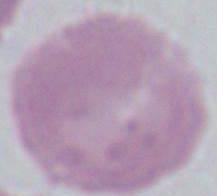
Summary:
  - Magnification: 1000x
  - Modality: photomicrograph
  - Identification: erythrocyte